Locate every blood parasite and identify its species.
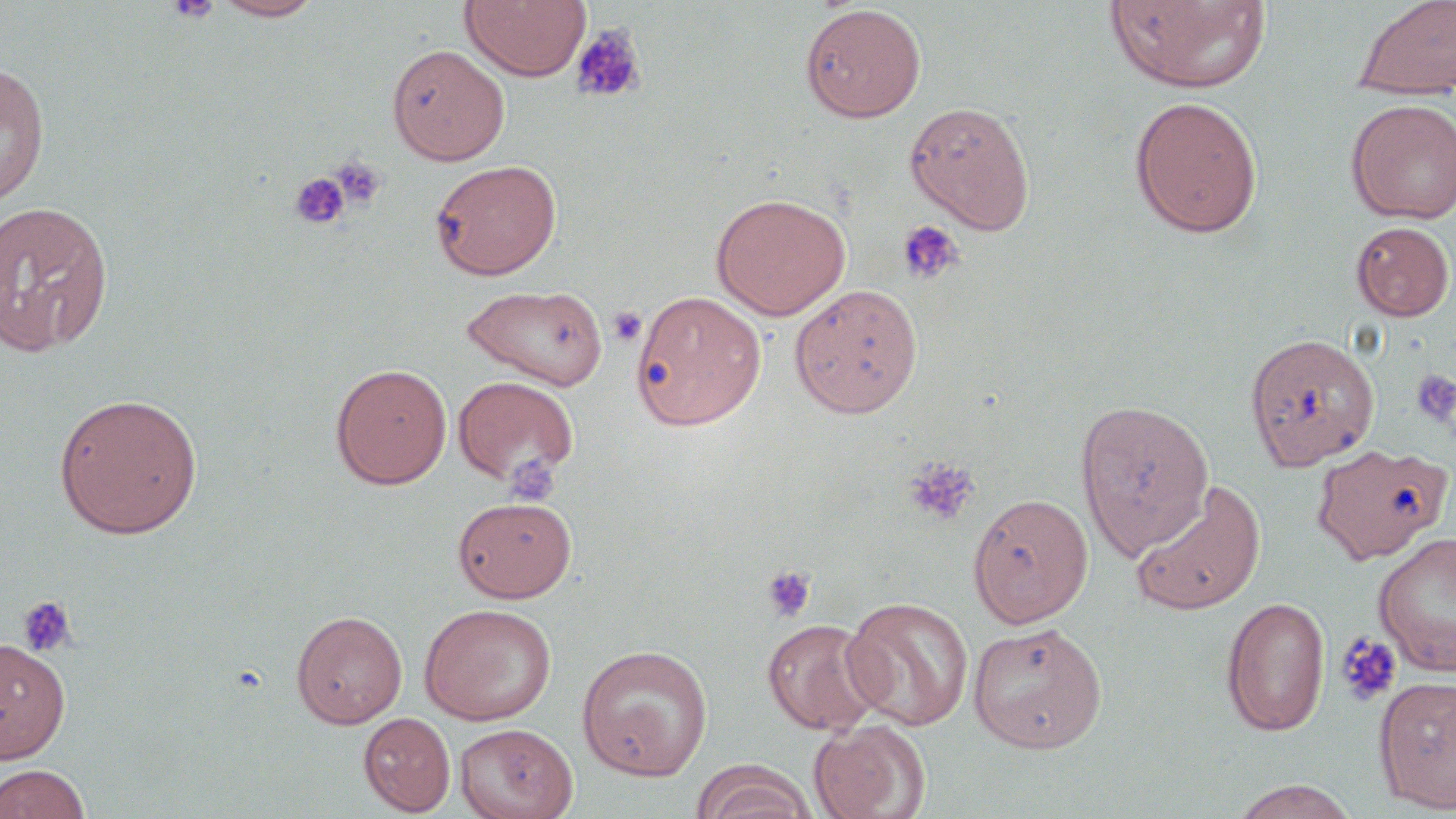
No blood parasites seen.

slide-level diagnosis = negative for blood parasites
modality = optical microscopy
field of view = single
preparation = thin blood film
platelet locations = approximate bounding boxes as [x1, y1, x2, y2] in pixels: [167, 0, 221, 23], [571, 23, 647, 104], [331, 156, 386, 209], [289, 172, 350, 230], [897, 220, 964, 285], [607, 306, 647, 348], [1410, 368, 1456, 428], [903, 457, 981, 526], [761, 564, 817, 624], [17, 595, 77, 657], [1335, 631, 1402, 706]
magnification = 1000x
image size = 1456×819 pixels
stain = May-Grünwald-Giemsa
uninfected red blood cell locations = approximate bounding boxes as [x1, y1, x2, y2] in pixels: [212, 0, 327, 21], [459, 0, 591, 82], [1104, 0, 1273, 94], [1352, 0, 1456, 101], [799, 4, 926, 123], [387, 44, 509, 165], [0, 62, 50, 206], [1128, 95, 1264, 239], [1345, 98, 1456, 224], [904, 100, 1036, 234], [430, 159, 562, 280], [711, 192, 850, 320], [0, 200, 114, 357], [1351, 220, 1454, 321], [462, 283, 609, 390], [789, 283, 923, 419], [630, 290, 765, 430], [1245, 332, 1380, 470], [330, 363, 452, 490], [452, 375, 579, 487], [53, 392, 204, 538], [1074, 397, 1214, 559], [1311, 443, 1451, 563], [1130, 480, 1266, 615], [968, 492, 1093, 627], [452, 496, 577, 602], [1373, 532, 1456, 676], [841, 596, 974, 730], [1221, 596, 1330, 737], [419, 603, 556, 725], [290, 609, 408, 729], [762, 618, 888, 736], [968, 622, 1107, 752], [0, 638, 71, 762], [576, 644, 713, 780], [1374, 676, 1456, 813], [358, 712, 455, 816], [809, 719, 929, 819], [455, 722, 578, 819], [694, 761, 816, 819], [0, 763, 92, 819], [1228, 778, 1361, 819]